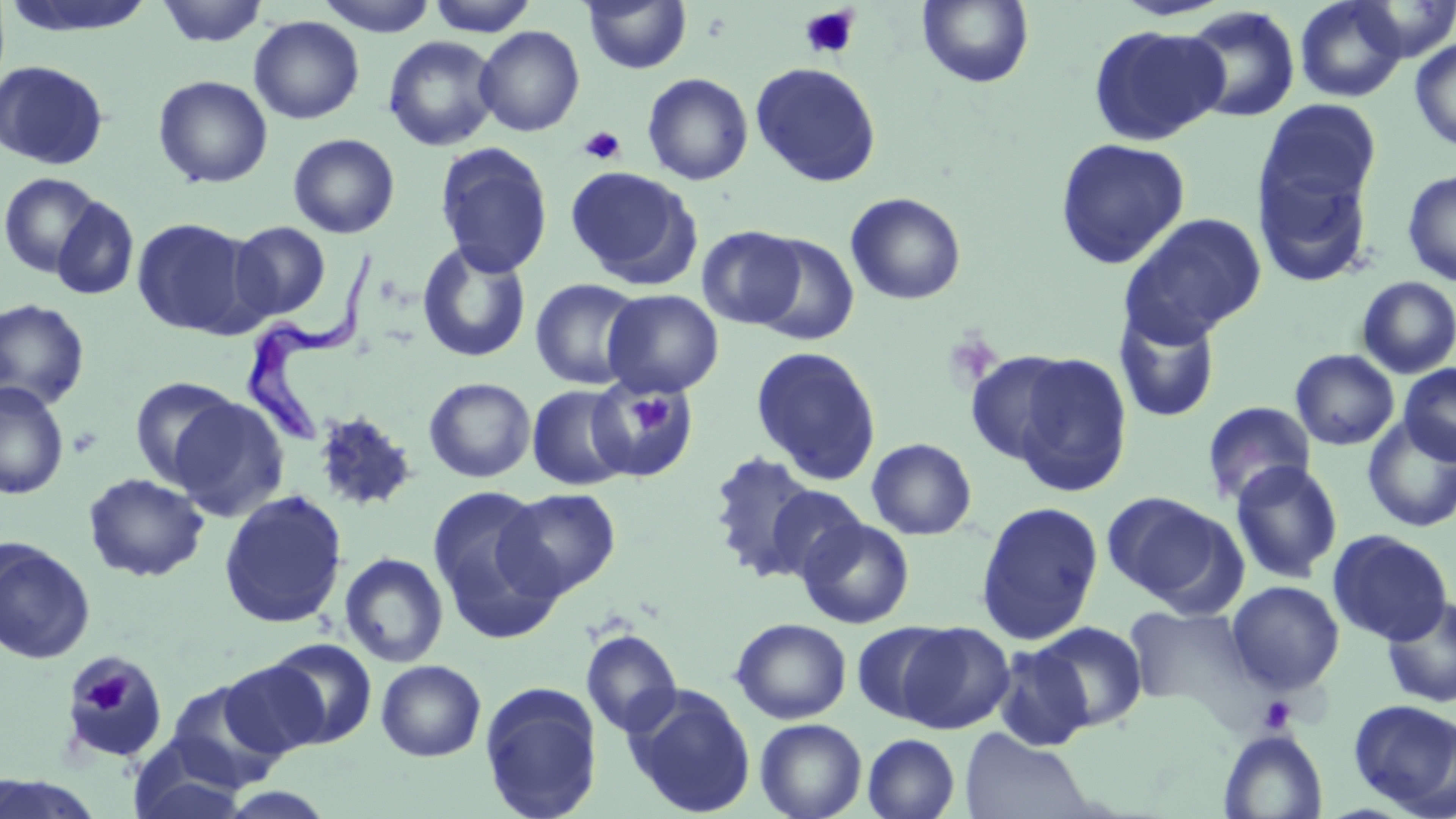 Approximate bounding boxes as (x1, y1, x2, y2) in pixels. Trypanosoma brucei locations: (245, 243, 383, 447). Platelet locations: (799, 6, 860, 60), (578, 125, 626, 165), (628, 395, 670, 436), (83, 671, 134, 714), (1259, 696, 1296, 734). Uninfected red blood cell locations: (155, 0, 269, 47), (316, 0, 439, 37), (426, 0, 539, 36), (917, 0, 1035, 88), (1294, 0, 1408, 103), (1350, 0, 1456, 61), (3, 1, 157, 39), (582, 1, 692, 74), (1181, 6, 1301, 123), (249, 16, 364, 124), (474, 25, 585, 137), (1089, 25, 1229, 146), (382, 35, 501, 152), (1409, 37, 1456, 152), (0, 60, 109, 170), (750, 62, 881, 187), (642, 73, 753, 185), (152, 75, 273, 189), (1257, 99, 1381, 219), (288, 133, 400, 239), (1054, 137, 1190, 269), (434, 142, 554, 277), (1255, 160, 1374, 289), (565, 166, 699, 286), (1402, 169, 1456, 287), (0, 172, 103, 277), (846, 192, 967, 305), (51, 196, 139, 301), (1119, 212, 1267, 344), (132, 217, 258, 338), (228, 221, 331, 322), (697, 225, 806, 329), (750, 233, 859, 345), (416, 240, 532, 364), (1356, 276, 1456, 379), (530, 278, 645, 389), (602, 289, 724, 397), (0, 299, 91, 411), (1115, 307, 1221, 423), (750, 346, 882, 484), (1290, 349, 1399, 450), (965, 350, 1080, 465), (1008, 352, 1133, 495), (1398, 363, 1456, 466), (129, 375, 243, 488), (424, 377, 536, 483), (0, 381, 70, 500), (588, 381, 698, 481), (527, 384, 632, 491), (167, 396, 288, 522), (1202, 401, 1315, 506), (312, 411, 419, 513), (1362, 417, 1456, 533), (866, 438, 976, 540), (706, 451, 824, 580), (1229, 460, 1344, 584), (83, 472, 209, 582), (427, 484, 564, 641), (762, 484, 869, 583), (499, 487, 622, 599), (218, 490, 348, 629), (1103, 492, 1240, 609), (975, 501, 1104, 644), (797, 517, 915, 629), (1327, 529, 1453, 646), (0, 537, 96, 664), (339, 552, 449, 668), (1226, 580, 1345, 694), (1382, 596, 1456, 708), (1125, 604, 1258, 713), (730, 618, 852, 724), (852, 621, 959, 725), (895, 621, 1015, 734), (1033, 621, 1148, 730), (580, 629, 682, 738), (264, 637, 379, 749), (991, 645, 1094, 752), (61, 654, 169, 764), (376, 659, 487, 762), (219, 660, 330, 759), (162, 679, 287, 793), (479, 682, 603, 819), (623, 684, 757, 817), (1348, 699, 1456, 815), (755, 718, 867, 819), (960, 730, 1094, 819), (1219, 730, 1328, 818), (862, 733, 961, 819), (128, 741, 249, 819), (0, 772, 105, 818). Slide-level diagnosis: Trypanosoma brucei. Optical microscopy. Thin blood film. Image is 1456×819 pixels. May-Grünwald-Giemsa stain. One field of a larger specimen. 1000x magnification.